Assess the morphology of the red blood cells.
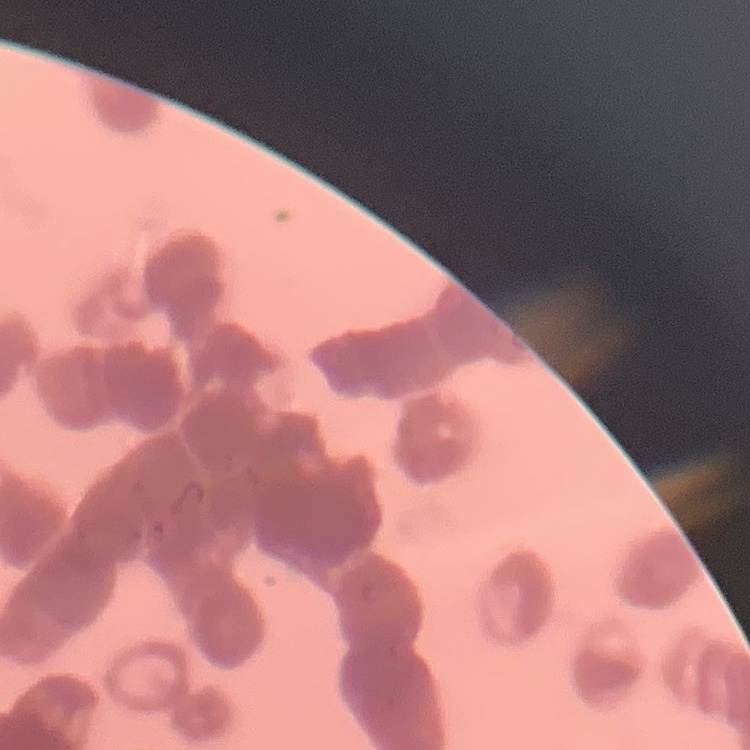

They show rouleaux formation.

Square crop of a larger photomicrograph. Thin blood film. Stained with either Field's or Giemsa.